Locate every Plasmodium parasite.
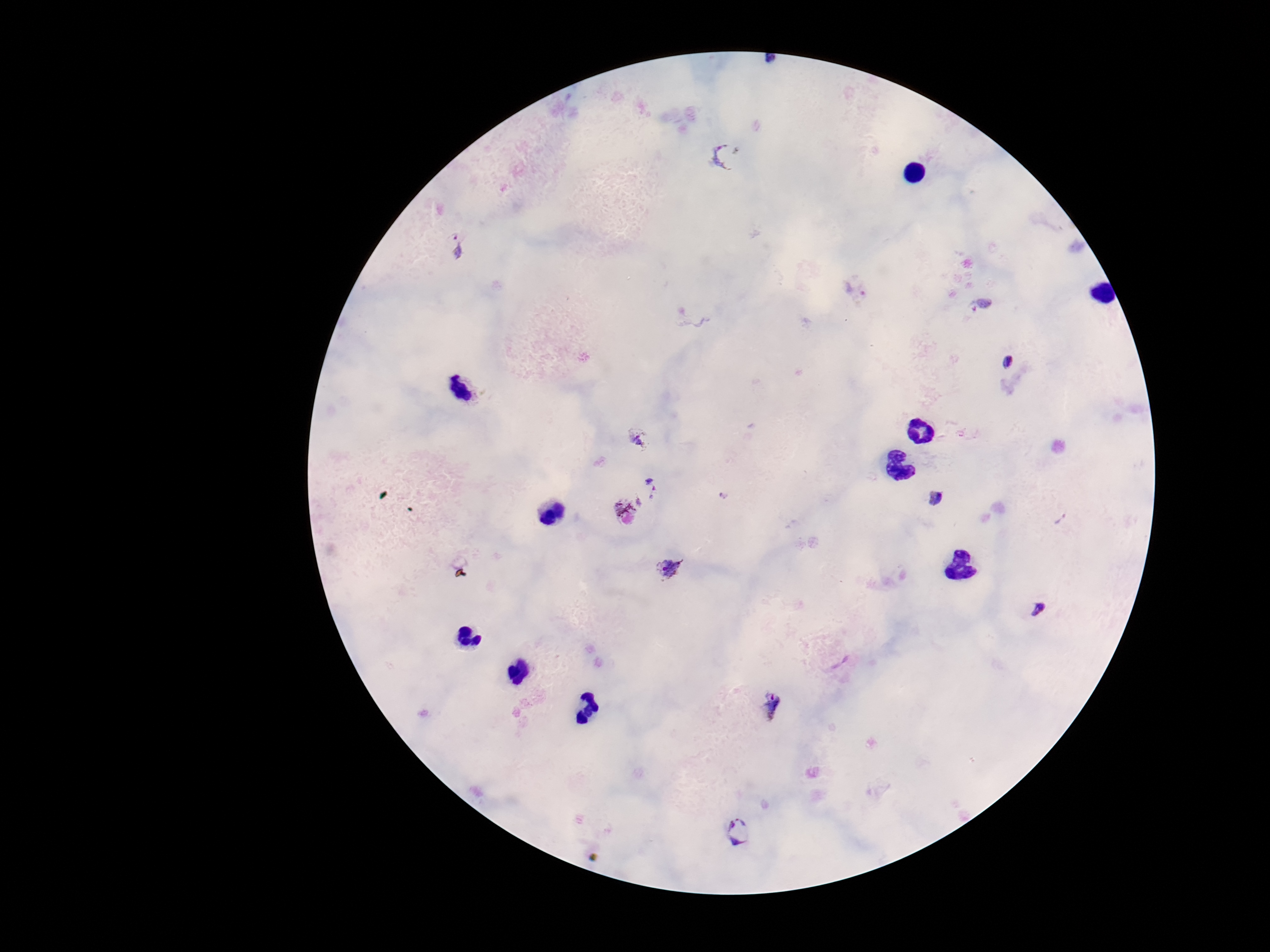
Approximate centers as [x, y] in pixels.
Plasmodium parasites: [726, 155], [458, 246], [857, 289], [979, 304], [1010, 364], [638, 438], [653, 487], [936, 498], [628, 511], [671, 571], [1039, 608], [769, 706], [740, 833].

Patient malaria status: positive. Photographed through the microscope eyepiece with a smartphone camera. Image is 1270×952 pixels. Thick peripheral-blood smear. Single field of view. 100x magnification. Giemsa stain.